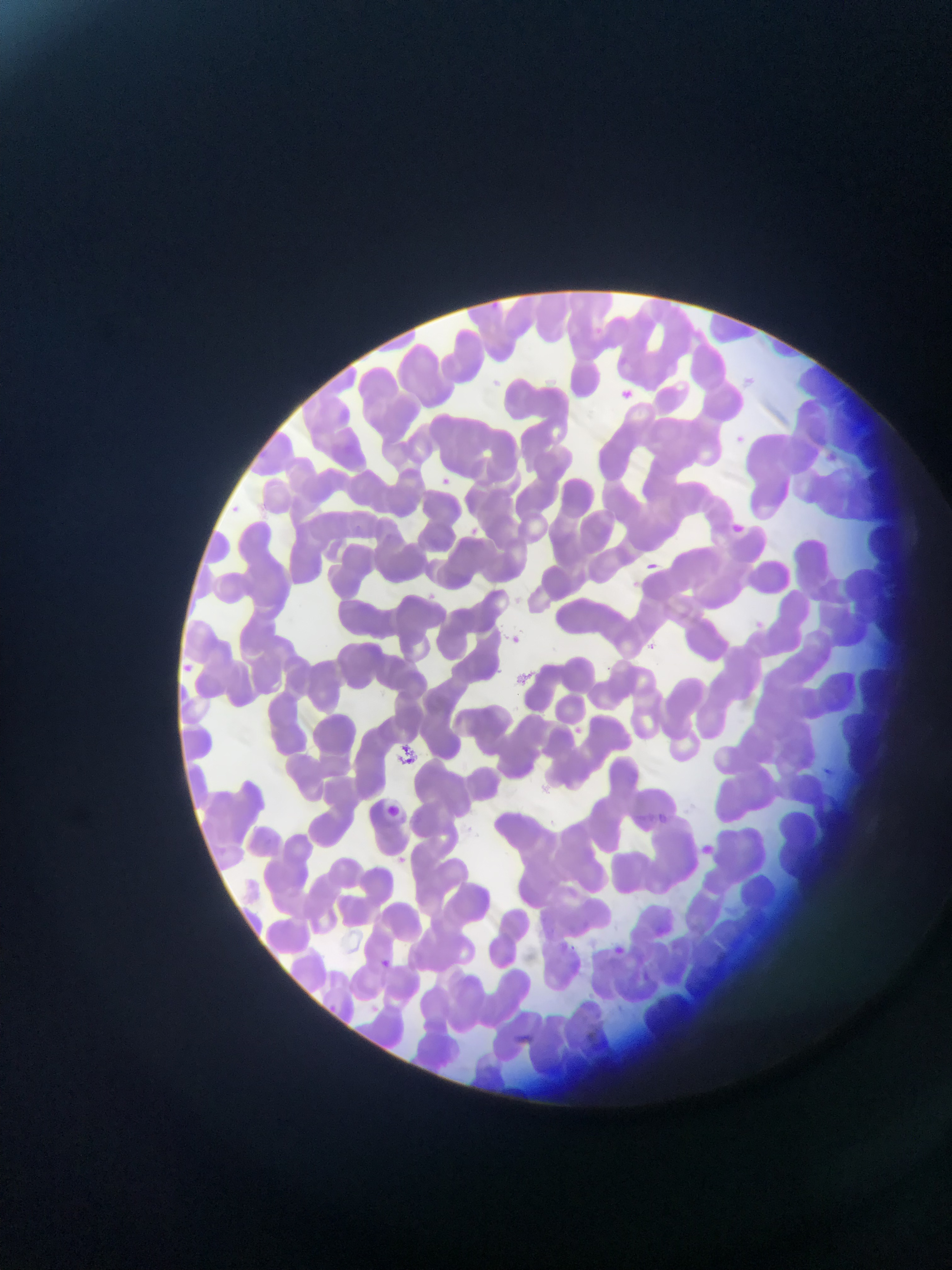
Approximate bounding boxes as {left, top, right, bottom} in pixels. Plasmodium parasite locations: {586, 326, 608, 343}, {615, 384, 638, 406}, {733, 433, 751, 455}, {437, 475, 453, 489}, {735, 516, 750, 546}, {348, 521, 365, 537}, {464, 524, 481, 539}, {641, 557, 665, 577}, {505, 631, 525, 650}, {647, 642, 658, 652}, {174, 658, 198, 680}, {823, 767, 835, 779}, {380, 802, 406, 828}, {657, 813, 669, 825}, {380, 958, 396, 975}, {328, 1001, 342, 1018}. Collected in Ghana. Image is 952×1270 pixels. Thin blood smear. One field of view. Mobile-phone photograph taken through the microscope.